Report the malaria status of this cell.
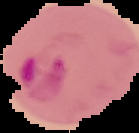

Parasitized.

Summary:
  - Preparation: thin blood film
  - Image size: 139×133 pixels
  - Image type: cell region segmented out of the field of view; surrounding area masked to black